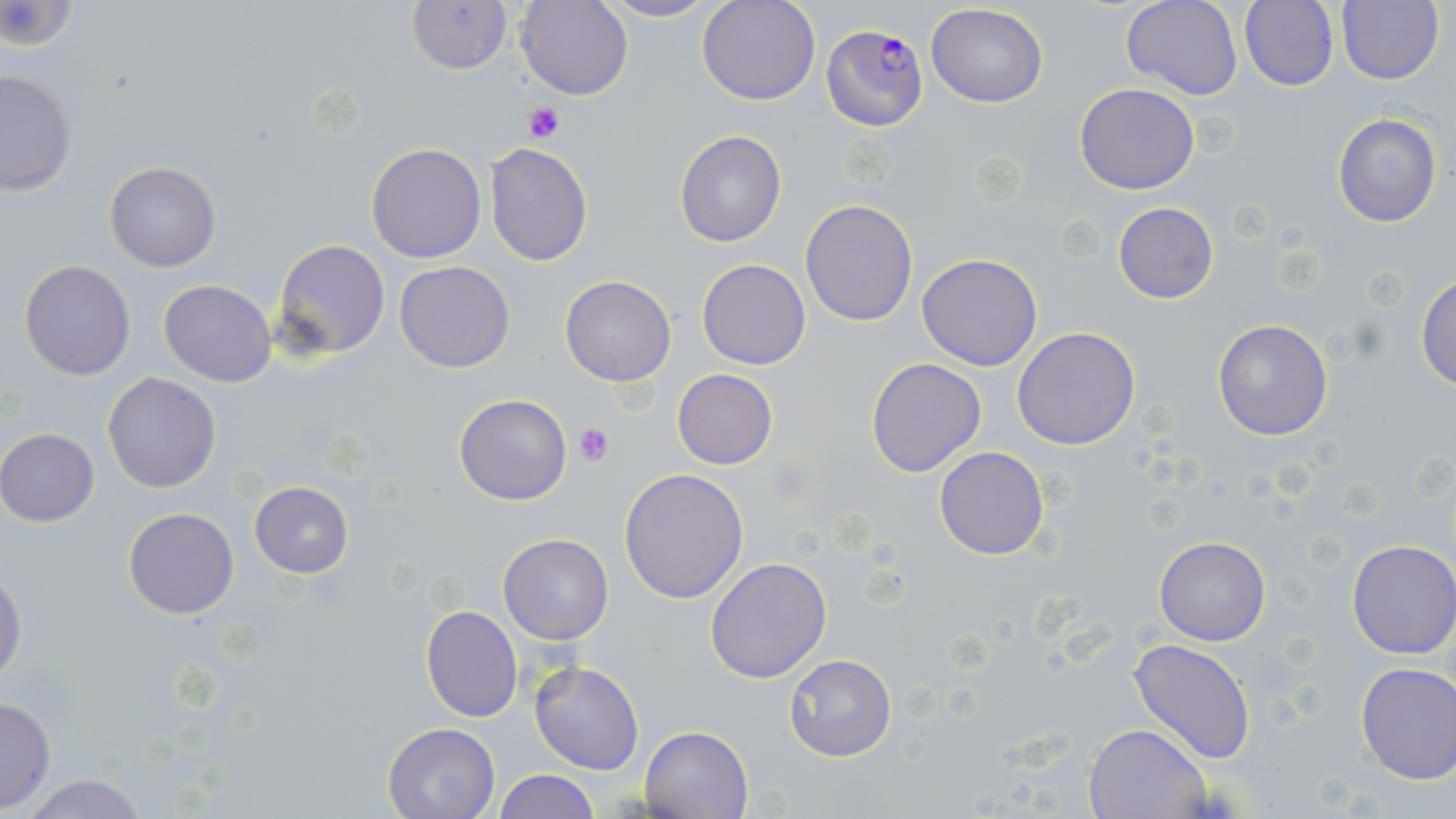

Approximate bounding boxes as (x1, y1, x2, y2) in pixels. Plasmodium falciparum-infected red blood cell locations: (820, 24, 928, 130). Uninfected red blood cell locations: (407, 0, 512, 74), (516, 0, 634, 101), (698, 0, 819, 105), (1121, 0, 1241, 101), (1338, 0, 1444, 86), (599, 1, 719, 23), (1238, 1, 1339, 90), (1, 2, 80, 54), (925, 4, 1049, 108), (1, 68, 76, 196), (1075, 83, 1199, 194), (1332, 111, 1442, 227), (674, 130, 786, 248), (366, 142, 487, 264), (486, 143, 593, 266), (104, 162, 221, 272), (800, 199, 917, 326), (1112, 202, 1219, 304), (272, 239, 390, 359), (916, 253, 1043, 371), (696, 259, 812, 370), (19, 260, 135, 381), (395, 260, 515, 373), (1416, 273, 1456, 390), (559, 277, 676, 386), (158, 280, 277, 386), (1211, 318, 1333, 440), (1012, 326, 1141, 450), (866, 357, 988, 477), (672, 369, 778, 470), (102, 372, 222, 493), (454, 393, 572, 506), (0, 428, 99, 526), (934, 447, 1048, 560), (619, 467, 749, 603), (248, 481, 354, 578), (123, 507, 239, 619), (497, 533, 615, 644), (1154, 536, 1271, 645), (1347, 539, 1456, 659), (704, 557, 832, 684), (0, 567, 25, 685), (421, 604, 524, 723), (1128, 638, 1257, 763), (784, 652, 897, 762), (529, 661, 644, 775), (1354, 661, 1455, 783), (0, 696, 55, 812), (382, 721, 501, 818), (1085, 723, 1210, 818), (640, 725, 754, 818), (495, 770, 599, 818), (17, 775, 152, 818). Platelet locations: (523, 101, 565, 142), (574, 424, 614, 465). Slide-level diagnosis: Plasmodium falciparum. Optical microscopy. Thin blood film. Image is 1456×819 pixels. May-Grünwald-Giemsa-stained preparation. Single field of view. 1000x magnification.